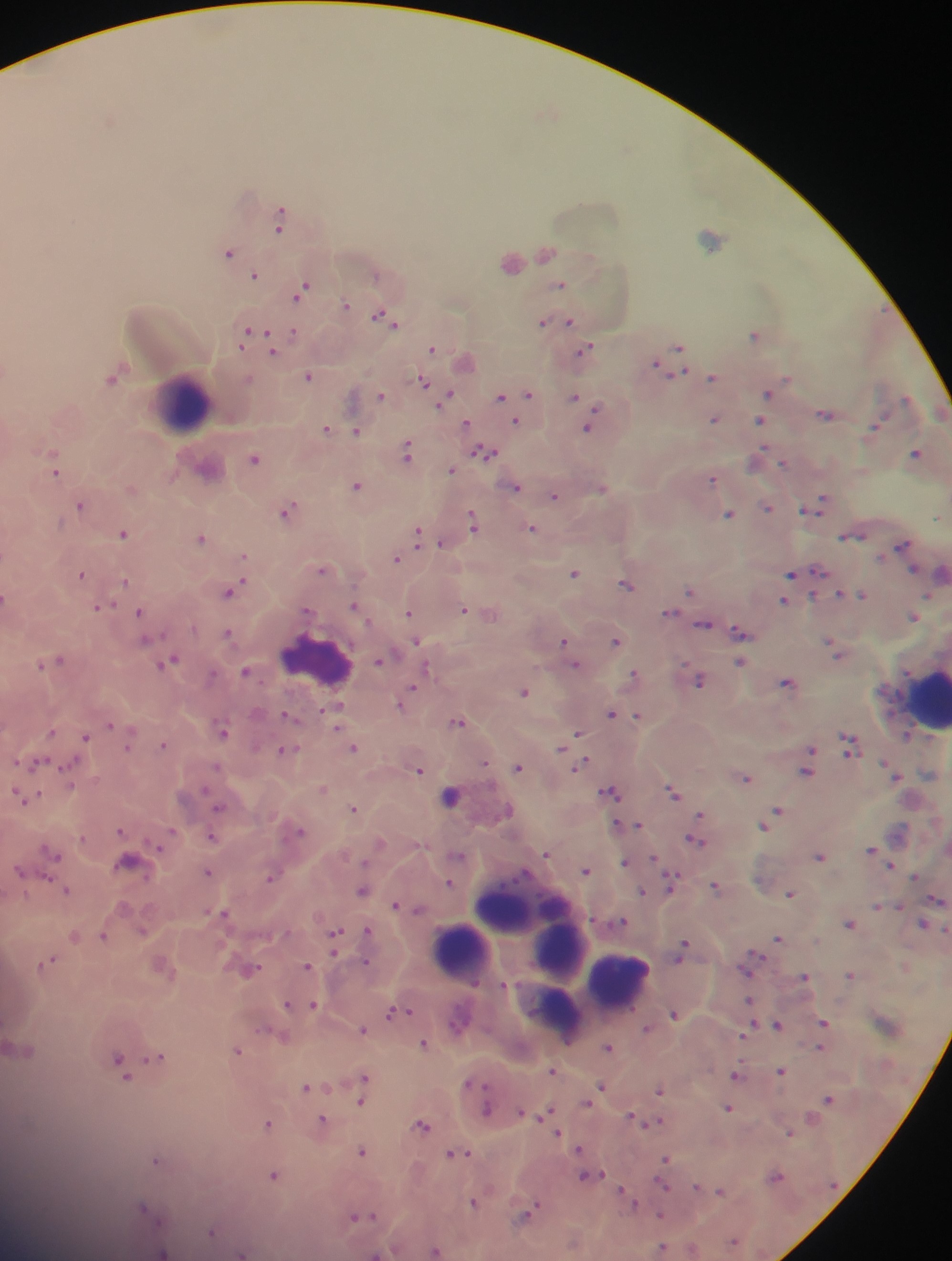
Approximate centers as (x, y) in pixels.
Summary:
  - Leukocyte locations: (180, 405), (316, 661), (928, 699), (448, 796), (520, 914), (559, 950), (459, 952), (618, 980)
  - Plasmodium parasite locations: (110, 120), (280, 215), (278, 230), (709, 238), (228, 252), (545, 253), (510, 262), (254, 275), (374, 275), (559, 285), (301, 290), (345, 304), (382, 316), (569, 321), (541, 322), (249, 333), (294, 333), (754, 335), (243, 340), (431, 348), (678, 348), (584, 350), (272, 352), (672, 362), (4, 370), (308, 376), (111, 377), (711, 378), (248, 379), (422, 381), (766, 393), (509, 394), (529, 394), (380, 395), (446, 397), (500, 397), (573, 398), (825, 414), (713, 418), (759, 421), (515, 422), (465, 423), (877, 424), (325, 428), (586, 429), (356, 430), (51, 452), (406, 452), (483, 453), (915, 453), (757, 458), (253, 459), (783, 463), (451, 470), (56, 473), (711, 479), (356, 486), (515, 487), (601, 489), (554, 496), (818, 503), (79, 505), (767, 508), (808, 508), (286, 510), (727, 515), (937, 517), (472, 522), (531, 528), (122, 533), (850, 535), (417, 536), (200, 537), (441, 543), (902, 545), (243, 556), (395, 558), (321, 569), (911, 569), (819, 572), (573, 573), (790, 573), (941, 573), (81, 574), (123, 582), (625, 584), (689, 590), (230, 591), (838, 595), (862, 595), (4, 597), (783, 601), (353, 605), (98, 607), (462, 609), (307, 610), (138, 612), (669, 612), (408, 613), (912, 616), (703, 625), (739, 632), (227, 634), (416, 641), (563, 641), (615, 641), (831, 645), (836, 654), (59, 659), (170, 660), (379, 660), (739, 662), (40, 663), (575, 665), (425, 669), (245, 671), (633, 673), (211, 676), (698, 681), (785, 682), (411, 689), (522, 692), (405, 698), (401, 705), (337, 707), (610, 714), (286, 716), (637, 716), (457, 722), (108, 725), (335, 728), (50, 732), (222, 732), (576, 734), (85, 737), (570, 739), (162, 744), (848, 744), (562, 746), (128, 747), (353, 747), (284, 750), (809, 751), (483, 763), (35, 764), (69, 765), (580, 765), (216, 766), (517, 767), (418, 770), (806, 771), (745, 778), (71, 786), (322, 788), (609, 792), (672, 792), (33, 797), (24, 800), (218, 807), (352, 809), (507, 811), (776, 811), (698, 814), (637, 825), (762, 825), (616, 826), (120, 830), (171, 831), (300, 832), (211, 837), (694, 842), (158, 846), (869, 849), (546, 853), (54, 855), (458, 856), (819, 856), (624, 862), (364, 863), (891, 865), (18, 870), (586, 870), (207, 871), (271, 875), (47, 877), (915, 877), (670, 880), (448, 883), (715, 887), (66, 890), (361, 890), (642, 891), (789, 894), (937, 900), (394, 904), (877, 905), (417, 909), (224, 913), (620, 921), (848, 924), (923, 924), (366, 931), (142, 932), (103, 936), (334, 936), (74, 937), (777, 938), (333, 947), (681, 950), (46, 962), (365, 962), (306, 966), (251, 969), (849, 974), (804, 976), (749, 1001), (285, 1004), (312, 1005), (390, 1012), (673, 1013), (822, 1023), (777, 1024), (644, 1028), (362, 1029), (262, 1030), (745, 1032), (282, 1037), (423, 1044), (608, 1047), (820, 1047), (237, 1051), (157, 1057), (119, 1064), (551, 1071), (781, 1071), (736, 1074), (364, 1077), (467, 1081), (304, 1086), (601, 1086), (658, 1091), (827, 1098), (360, 1102), (586, 1103), (727, 1108), (485, 1109), (521, 1112), (546, 1112), (632, 1117), (321, 1120), (652, 1122), (267, 1123), (421, 1125), (557, 1133), (789, 1133), (578, 1149), (362, 1152), (455, 1153), (665, 1158), (155, 1161), (272, 1175), (585, 1176), (775, 1176), (664, 1187), (695, 1187), (720, 1191), (622, 1193), (628, 1199), (472, 1202), (143, 1207), (526, 1214), (660, 1216), (354, 1217), (370, 1217), (211, 1231), (732, 1241), (661, 1249), (691, 1250), (435, 1251), (163, 1252), (241, 1254), (374, 1254)
  - Image size: 952×1261 pixels
  - Preparation: thick blood film
  - Field of view: single
  - Country: Ghana
  - Capture: mobile-phone photograph through a microscope